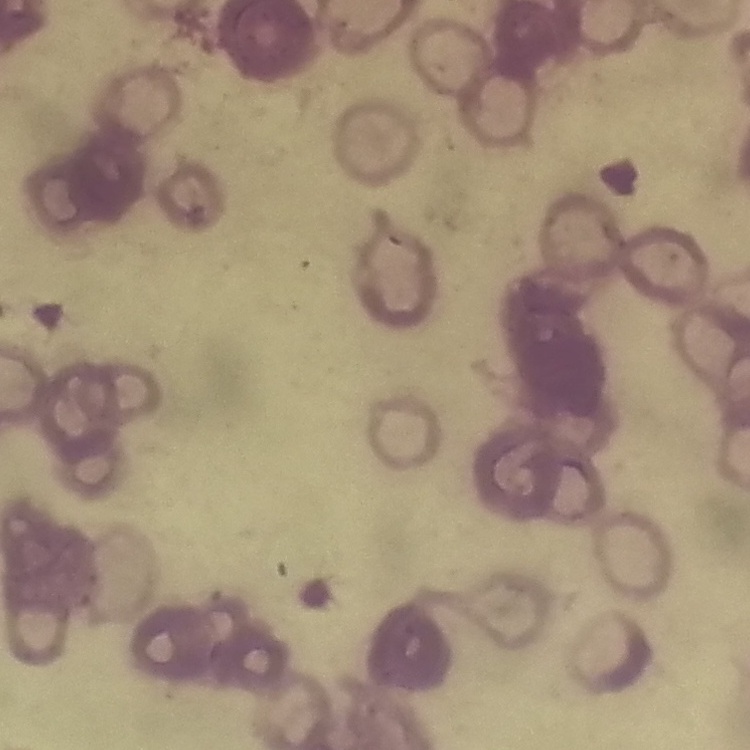
Summary:
  - Erythrocyte morphology: rouleaux formation
  - Image type: one tile cut from a larger photomicrograph
  - Stain: Field's or Giemsa
  - Preparation: thin blood smear